Identify the parasite.
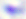
Toxoplasma gondii.

Summary:
  - Modality: photomicrograph
  - Magnification: 400x